Outline each blood parasite and name the species.
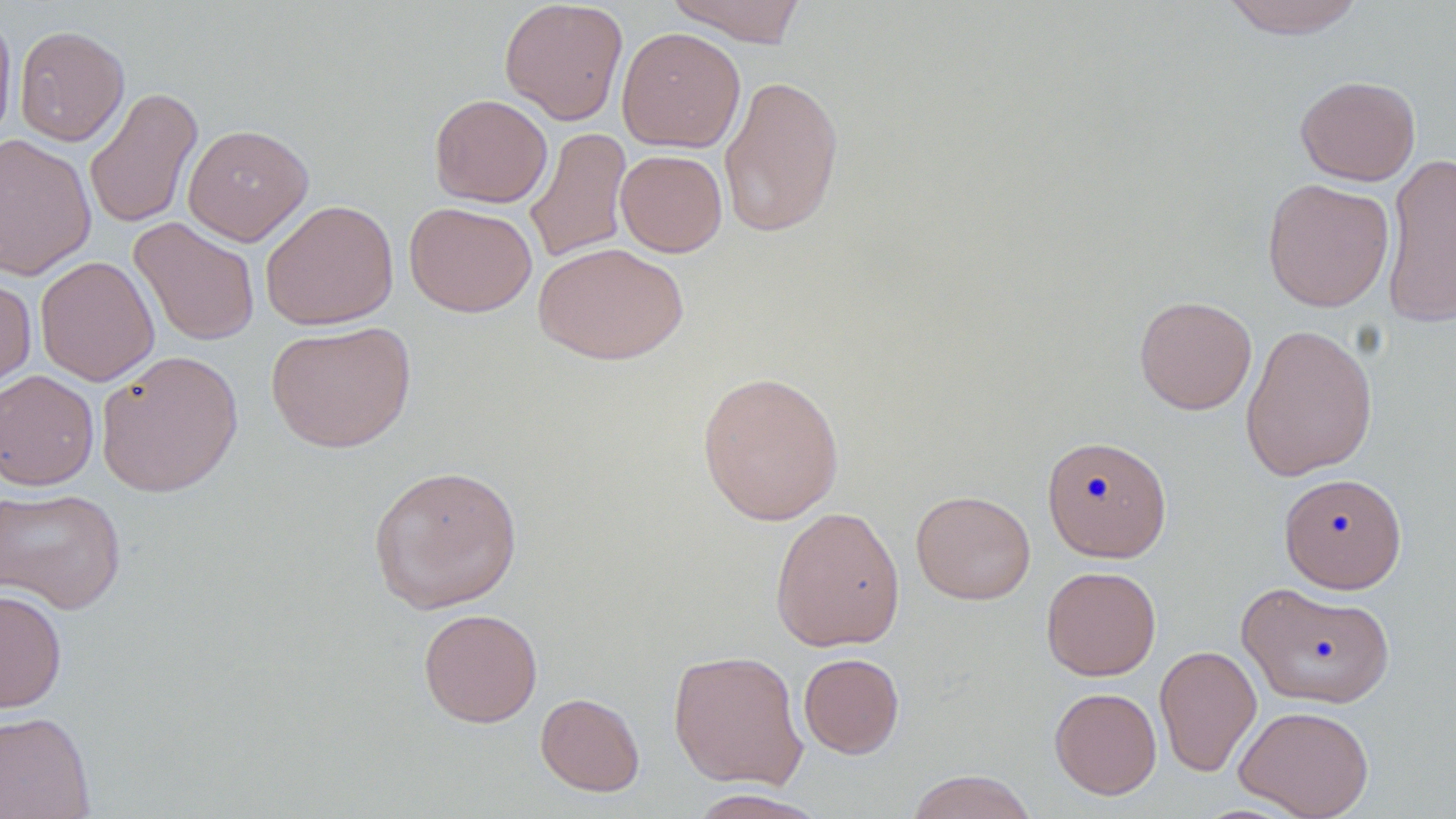

No blood parasites observed.

slide_level_diagnosis: negative for blood parasites
preparation: thin blood film
magnification: 1000x
field_of_view: single
stain: May-Grünwald-Giemsa
uninfected_red_blood_cell_locations: 'approximate bounding boxes as named x1/y1/x2/y2 corners in pixels: (x1=498, y1=0, x2=629, y2=125), (x1=664, y1=0, x2=809, y2=45), (x1=1220, y1=0, x2=1368, y2=38), (x1=0, y1=5, x2=17, y2=148), (x1=14, y1=25, x2=130, y2=147), (x1=616, y1=26, x2=745, y2=153), (x1=718, y1=74, x2=845, y2=238), (x1=1295, y1=75, x2=1421, y2=186), (x1=84, y1=86, x2=202, y2=230), (x1=429, y1=94, x2=553, y2=207), (x1=183, y1=123, x2=314, y2=245), (x1=525, y1=126, x2=633, y2=264), (x1=0, y1=133, x2=96, y2=281), (x1=615, y1=149, x2=728, y2=257), (x1=1381, y1=151, x2=1456, y2=329), (x1=1261, y1=178, x2=1394, y2=312), (x1=260, y1=199, x2=399, y2=330), (x1=404, y1=201, x2=537, y2=317), (x1=129, y1=216, x2=260, y2=347), (x1=532, y1=242, x2=689, y2=365), (x1=35, y1=255, x2=160, y2=386), (x1=0, y1=274, x2=37, y2=394), (x1=1134, y1=295, x2=1257, y2=415), (x1=265, y1=320, x2=416, y2=453), (x1=1240, y1=322, x2=1379, y2=481), (x1=95, y1=349, x2=244, y2=498), (x1=0, y1=370, x2=100, y2=491), (x1=696, y1=370, x2=845, y2=526), (x1=1041, y1=434, x2=1172, y2=562), (x1=368, y1=463, x2=523, y2=614), (x1=1279, y1=472, x2=1407, y2=593), (x1=0, y1=486, x2=127, y2=614), (x1=910, y1=490, x2=1036, y2=604), (x1=769, y1=505, x2=905, y2=652), (x1=1041, y1=565, x2=1161, y2=681), (x1=1237, y1=581, x2=1395, y2=708), (x1=0, y1=587, x2=68, y2=713), (x1=418, y1=608, x2=543, y2=727), (x1=1154, y1=645, x2=1262, y2=776), (x1=668, y1=649, x2=808, y2=789), (x1=798, y1=653, x2=905, y2=759), (x1=1049, y1=686, x2=1162, y2=799), (x1=535, y1=692, x2=645, y2=796), (x1=1234, y1=704, x2=1374, y2=819), (x1=0, y1=710, x2=96, y2=819), (x1=905, y1=769, x2=1038, y2=819), (x1=685, y1=789, x2=831, y2=818)'
modality: optical microscopy
image_size: 1456×819 pixels